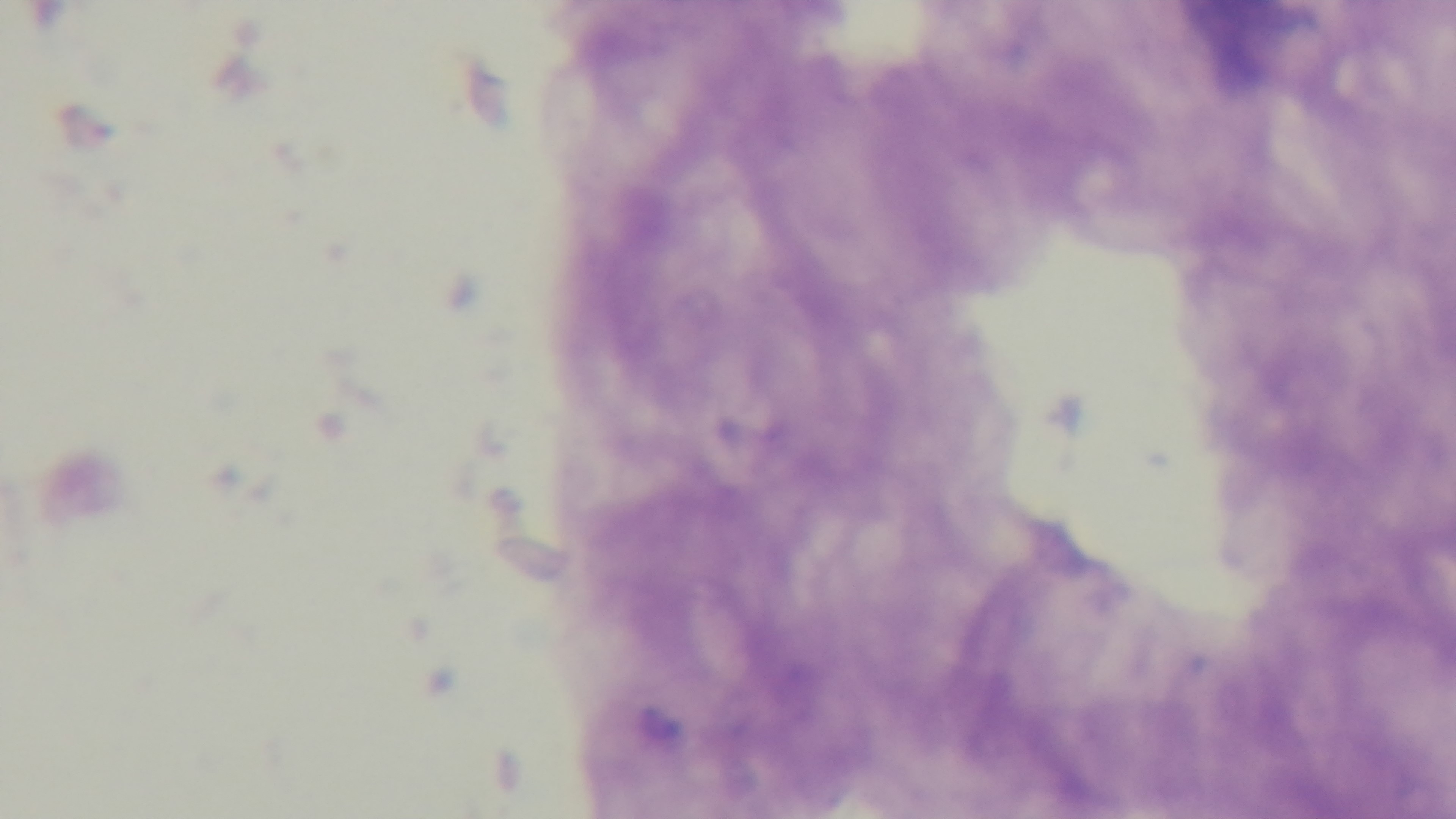
Summary:
  - Objective: 100x oil immersion
  - Stain: Giemsa
  - Capture: mounted 4K digital camera
  - Malaria status: negative
  - Preparation: thick blood film
  - Modality: light microscopy
  - Field of view: one from the slide